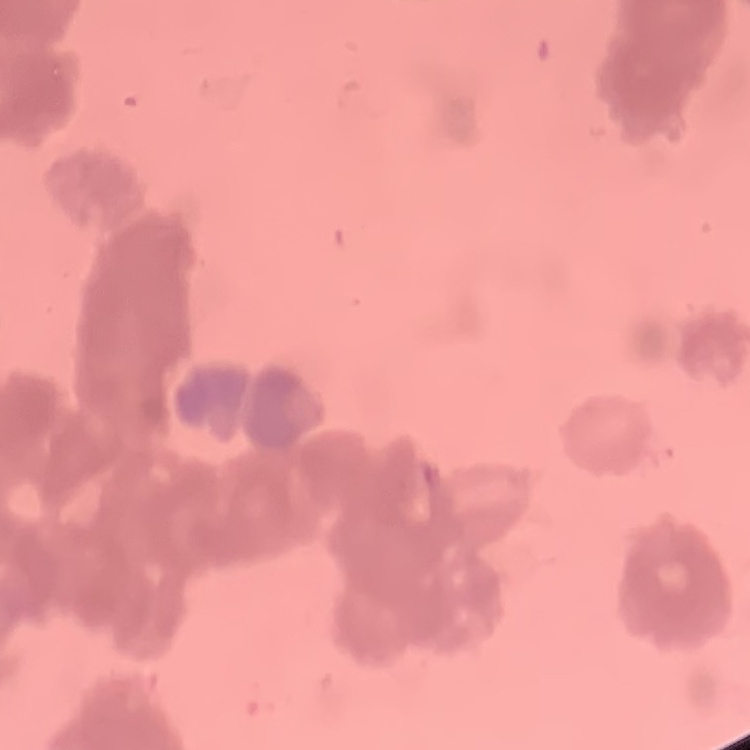 The erythrocytes show rouleaux formation. Thin blood film. Field's or Giemsa stain. One tile cut from a larger photomicrograph.